Describe the morphology of the red blood cells.
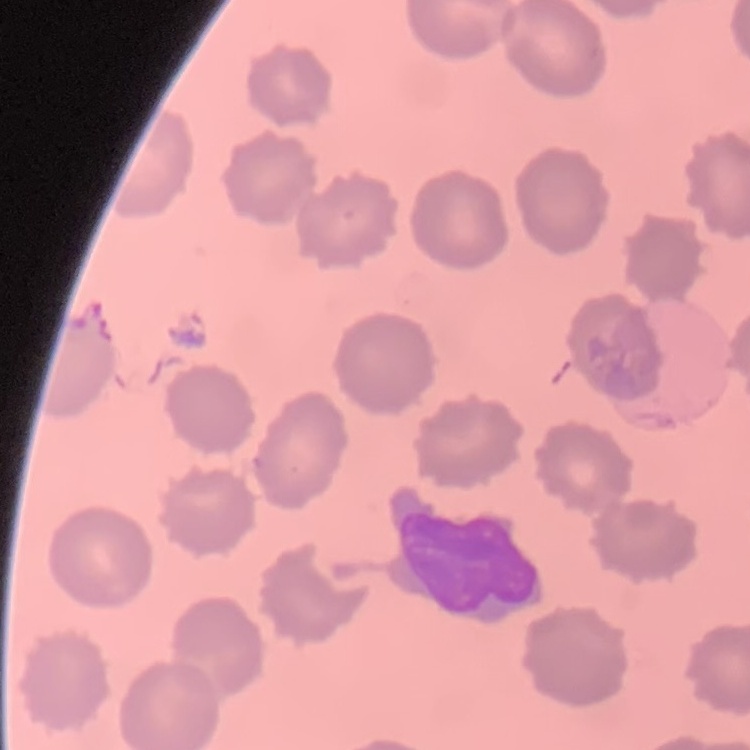
They show no rouleaux formation.

preparation = thin blood smear
stain = Field's or Giemsa
image type = square crop of a larger photomicrograph